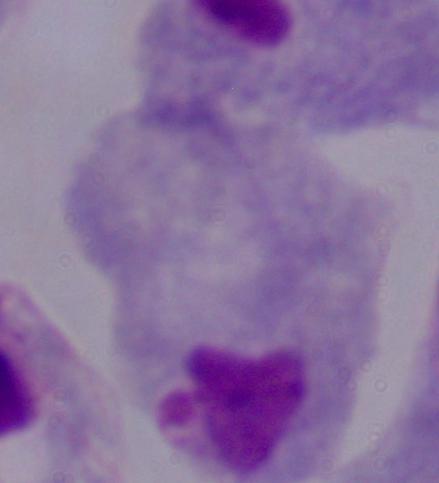
Summary:
  - Magnification: 1000x
  - Modality: photomicrograph
  - Identification: trichomonad